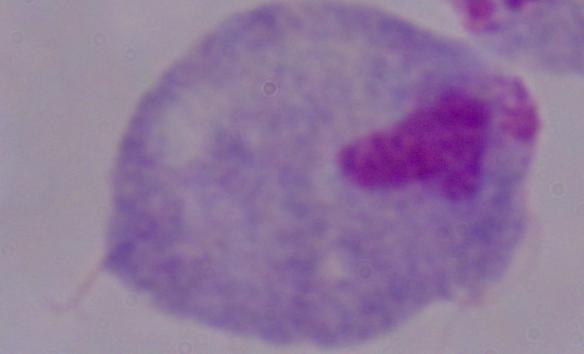

A trichomonad is shown. Micrograph. 1000x magnification.